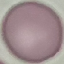

Summary:
  - Result: no malaria parasites detected
  - Preparation: thin smear
  - Stain: Giemsa
  - Image type: automatically extracted cell patch, resized to 64 × 64 pixels
  - Capture: smartphone through the microscope eyepiece